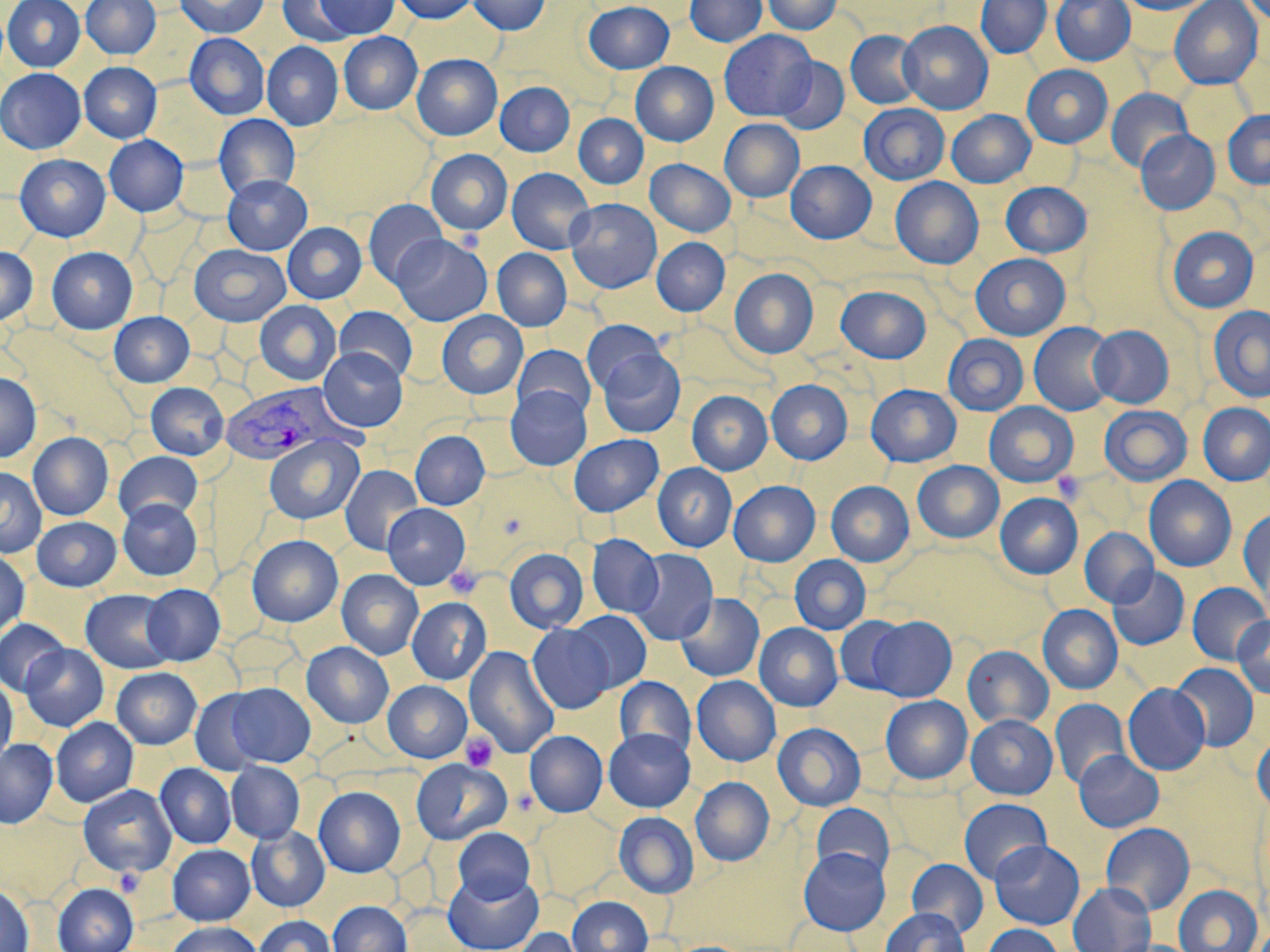
Summary:
  - Coordinate format: approximate bounding boxes as named x1/y1/x2/y2 corners in pixels
  - Uninfected red blood cell locations: (x1=3, y1=0, x2=85, y2=72), (x1=81, y1=0, x2=161, y2=59), (x1=175, y1=0, x2=269, y2=38), (x1=277, y1=0, x2=360, y2=46), (x1=312, y1=0, x2=400, y2=38), (x1=392, y1=0, x2=479, y2=23), (x1=469, y1=0, x2=550, y2=35), (x1=685, y1=0, x2=767, y2=46), (x1=762, y1=0, x2=841, y2=34), (x1=976, y1=0, x2=1052, y2=58), (x1=1051, y1=0, x2=1135, y2=65), (x1=1119, y1=0, x2=1216, y2=15), (x1=1169, y1=0, x2=1263, y2=89), (x1=1240, y1=0, x2=1270, y2=26), (x1=584, y1=1, x2=674, y2=73), (x1=899, y1=21, x2=993, y2=114), (x1=719, y1=30, x2=817, y2=120), (x1=845, y1=30, x2=924, y2=110), (x1=339, y1=32, x2=422, y2=114), (x1=185, y1=33, x2=269, y2=120), (x1=262, y1=42, x2=343, y2=130), (x1=412, y1=54, x2=501, y2=140), (x1=774, y1=57, x2=850, y2=134), (x1=79, y1=62, x2=162, y2=142), (x1=631, y1=62, x2=718, y2=145), (x1=1022, y1=64, x2=1112, y2=148), (x1=0, y1=68, x2=86, y2=154), (x1=495, y1=81, x2=574, y2=156), (x1=1106, y1=89, x2=1193, y2=173), (x1=859, y1=103, x2=949, y2=185), (x1=947, y1=110, x2=1035, y2=187), (x1=1222, y1=110, x2=1270, y2=189), (x1=214, y1=114, x2=300, y2=199), (x1=574, y1=114, x2=648, y2=188), (x1=720, y1=119, x2=804, y2=202), (x1=1136, y1=130, x2=1220, y2=214), (x1=104, y1=135, x2=188, y2=216), (x1=426, y1=149, x2=513, y2=235), (x1=14, y1=154, x2=110, y2=241), (x1=646, y1=159, x2=736, y2=237), (x1=786, y1=160, x2=876, y2=243), (x1=507, y1=167, x2=595, y2=254), (x1=222, y1=175, x2=311, y2=255), (x1=891, y1=177, x2=983, y2=269), (x1=1000, y1=182, x2=1092, y2=258), (x1=363, y1=199, x2=448, y2=287), (x1=565, y1=199, x2=662, y2=293), (x1=282, y1=222, x2=367, y2=304), (x1=1167, y1=226, x2=1259, y2=313), (x1=390, y1=234, x2=492, y2=326), (x1=652, y1=238, x2=729, y2=315), (x1=190, y1=244, x2=291, y2=326), (x1=0, y1=247, x2=37, y2=325), (x1=46, y1=247, x2=137, y2=333), (x1=492, y1=248, x2=571, y2=331), (x1=970, y1=253, x2=1070, y2=340), (x1=729, y1=268, x2=818, y2=358), (x1=836, y1=285, x2=932, y2=363), (x1=255, y1=300, x2=342, y2=386), (x1=334, y1=306, x2=417, y2=382), (x1=1208, y1=306, x2=1270, y2=402), (x1=437, y1=311, x2=527, y2=399), (x1=109, y1=312, x2=194, y2=387), (x1=582, y1=319, x2=667, y2=394), (x1=1029, y1=323, x2=1117, y2=416), (x1=1088, y1=325, x2=1174, y2=408), (x1=943, y1=334, x2=1028, y2=415), (x1=513, y1=344, x2=595, y2=420), (x1=319, y1=347, x2=407, y2=431), (x1=597, y1=349, x2=685, y2=437), (x1=0, y1=372, x2=41, y2=462), (x1=766, y1=379, x2=852, y2=464), (x1=146, y1=382, x2=229, y2=459), (x1=866, y1=384, x2=961, y2=467), (x1=506, y1=386, x2=592, y2=470), (x1=687, y1=390, x2=772, y2=475), (x1=984, y1=402, x2=1078, y2=487), (x1=1198, y1=402, x2=1270, y2=485), (x1=1099, y1=404, x2=1192, y2=486), (x1=410, y1=430, x2=489, y2=510), (x1=28, y1=432, x2=113, y2=520), (x1=264, y1=434, x2=363, y2=524), (x1=569, y1=434, x2=663, y2=516), (x1=114, y1=451, x2=202, y2=525), (x1=913, y1=461, x2=1003, y2=543), (x1=653, y1=463, x2=737, y2=551), (x1=340, y1=465, x2=423, y2=555), (x1=0, y1=466, x2=46, y2=558), (x1=1144, y1=476, x2=1236, y2=572), (x1=729, y1=480, x2=820, y2=566), (x1=826, y1=481, x2=914, y2=566), (x1=995, y1=493, x2=1082, y2=578), (x1=118, y1=498, x2=202, y2=580), (x1=383, y1=503, x2=470, y2=589), (x1=1239, y1=509, x2=1270, y2=600), (x1=32, y1=516, x2=121, y2=591), (x1=1079, y1=528, x2=1158, y2=608), (x1=247, y1=534, x2=343, y2=627), (x1=587, y1=534, x2=664, y2=618), (x1=504, y1=548, x2=589, y2=633), (x1=629, y1=548, x2=718, y2=645), (x1=0, y1=551, x2=29, y2=638), (x1=790, y1=555, x2=871, y2=634), (x1=1107, y1=567, x2=1189, y2=651), (x1=337, y1=569, x2=423, y2=659), (x1=1187, y1=582, x2=1269, y2=665), (x1=142, y1=584, x2=225, y2=665), (x1=81, y1=589, x2=176, y2=673), (x1=676, y1=593, x2=764, y2=682), (x1=407, y1=597, x2=491, y2=685), (x1=1038, y1=604, x2=1123, y2=694), (x1=568, y1=610, x2=652, y2=693), (x1=1233, y1=615, x2=1270, y2=699), (x1=834, y1=616, x2=910, y2=695), (x1=865, y1=616, x2=957, y2=701), (x1=0, y1=619, x2=70, y2=695), (x1=754, y1=623, x2=843, y2=711), (x1=527, y1=624, x2=614, y2=713), (x1=302, y1=642, x2=393, y2=728), (x1=20, y1=643, x2=108, y2=731), (x1=963, y1=645, x2=1053, y2=730), (x1=464, y1=646, x2=559, y2=758), (x1=1171, y1=663, x2=1258, y2=752), (x1=112, y1=667, x2=201, y2=749), (x1=614, y1=676, x2=695, y2=759), (x1=692, y1=676, x2=780, y2=766), (x1=0, y1=677, x2=17, y2=764), (x1=383, y1=680, x2=471, y2=762), (x1=224, y1=682, x2=315, y2=767), (x1=1123, y1=683, x2=1210, y2=775), (x1=189, y1=689, x2=268, y2=775), (x1=881, y1=695, x2=972, y2=784), (x1=1050, y1=698, x2=1130, y2=789), (x1=966, y1=714, x2=1058, y2=799), (x1=51, y1=717, x2=138, y2=807), (x1=773, y1=723, x2=866, y2=811), (x1=604, y1=729, x2=695, y2=812), (x1=525, y1=730, x2=607, y2=817), (x1=1252, y1=735, x2=1270, y2=811), (x1=0, y1=739, x2=57, y2=828), (x1=1074, y1=750, x2=1164, y2=832), (x1=411, y1=759, x2=510, y2=844), (x1=226, y1=762, x2=304, y2=843), (x1=155, y1=763, x2=236, y2=848), (x1=691, y1=777, x2=774, y2=866), (x1=78, y1=785, x2=176, y2=877), (x1=314, y1=786, x2=405, y2=877), (x1=959, y1=798, x2=1052, y2=883), (x1=811, y1=802, x2=895, y2=880), (x1=532, y1=809, x2=622, y2=899), (x1=614, y1=811, x2=698, y2=898), (x1=1101, y1=822, x2=1195, y2=915), (x1=246, y1=826, x2=330, y2=911), (x1=453, y1=827, x2=536, y2=904), (x1=989, y1=840, x2=1084, y2=929), (x1=168, y1=844, x2=255, y2=925), (x1=798, y1=847, x2=890, y2=935), (x1=907, y1=858, x2=988, y2=937), (x1=444, y1=870, x2=543, y2=952), (x1=1068, y1=882, x2=1156, y2=952), (x1=52, y1=883, x2=138, y2=952), (x1=0, y1=884, x2=33, y2=952), (x1=1173, y1=884, x2=1262, y2=952), (x1=567, y1=896, x2=652, y2=952), (x1=328, y1=901, x2=411, y2=952), (x1=881, y1=907, x2=969, y2=952), (x1=254, y1=915, x2=336, y2=952), (x1=166, y1=921, x2=264, y2=952), (x1=982, y1=924, x2=1064, y2=952), (x1=511, y1=927, x2=586, y2=952)
  - Platelet locations: (x1=1053, y1=471, x2=1087, y2=504), (x1=445, y1=566, x2=482, y2=599), (x1=460, y1=732, x2=497, y2=771)
  - Plasmodium vivax-infected red blood cell locations: (x1=219, y1=383, x2=354, y2=466)
  - Slide-level diagnosis: Plasmodium vivax
  - Stain: May-Grünwald-Giemsa
  - Modality: light microscopy
  - Preparation: thin blood smear
  - Magnification: 1000x
  - Image size: 1270×952 pixels
  - Field of view: single